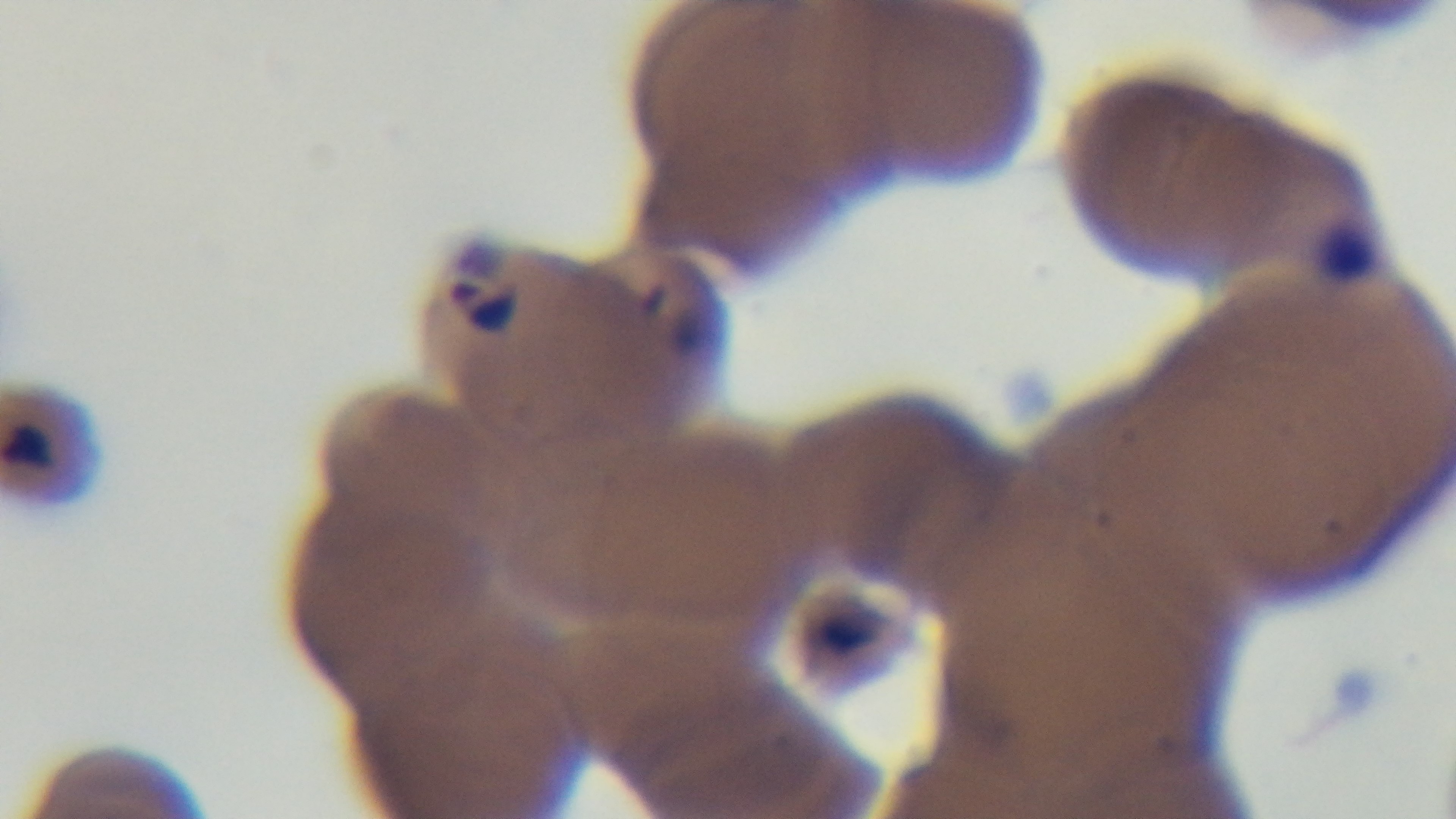
preparation = thin smear
field of view = single
modality = light microscopy
malaria status = positive
capture = mounted 4K digital camera
objective = 100x oil immersion
stain = Giemsa